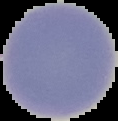
From a thin blood smear. Cell region segmented out of the field of view; the surrounding area is masked to black. Malaria status: uninfected. Image is 118×121 pixels.